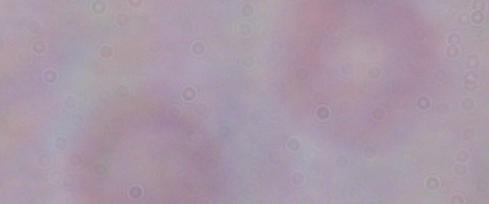

A trypanosome is seen. Photomicrograph. Captured at 1000x magnification.